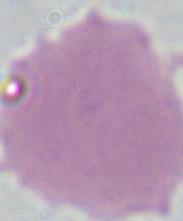

A red blood cell is shown. 1000x magnification. Micrograph.